State the preparation type.
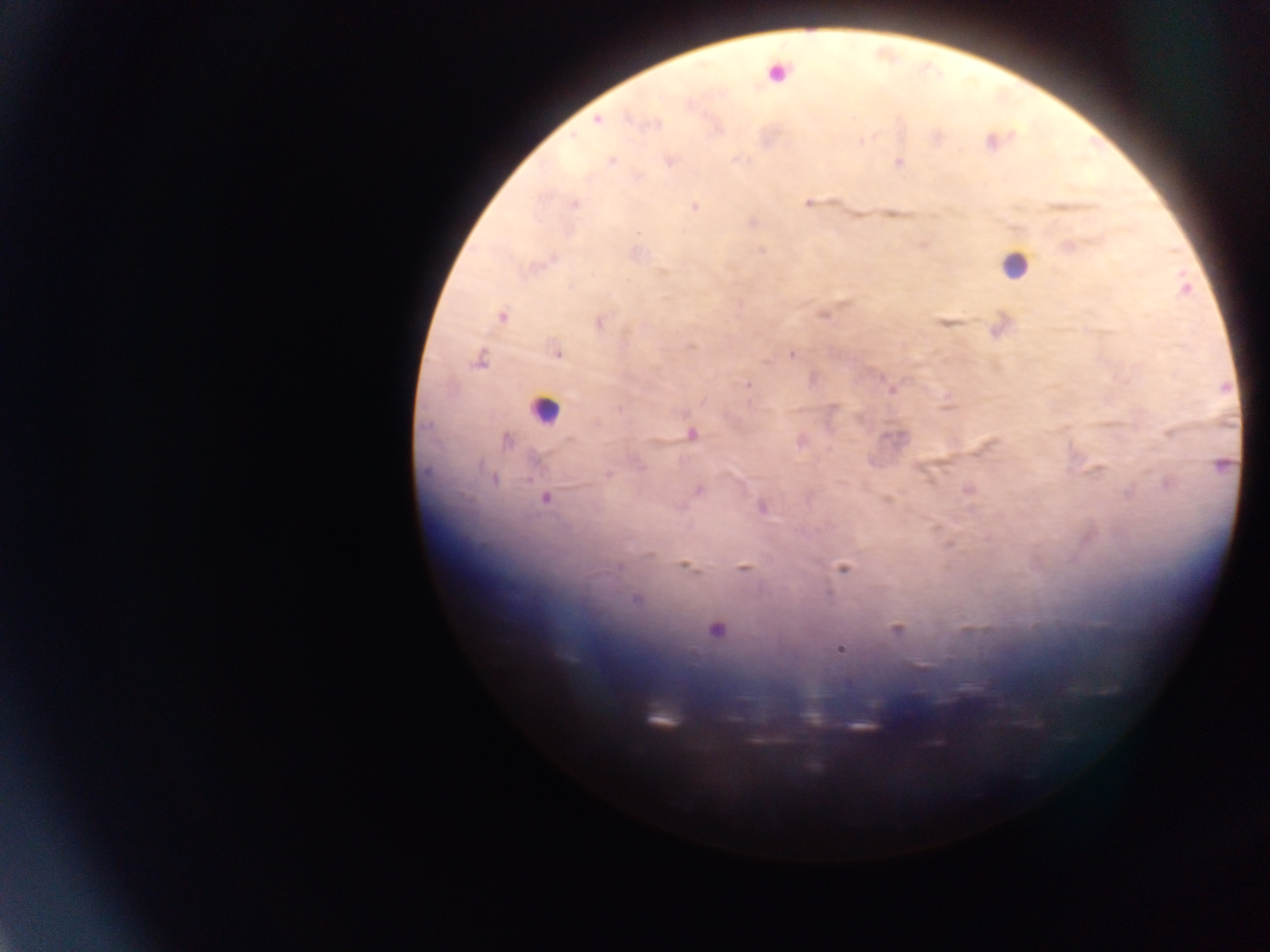

Thick blood film.

Approximate centers as (x, y) in pixels.
Summary:
  - Leukocyte locations: (779, 72), (1015, 264), (544, 409)
  - Malaria parasite locations: (597, 119), (652, 124), (935, 136), (863, 139), (992, 142), (669, 160), (611, 161), (899, 162), (638, 177), (806, 202), (573, 203), (695, 207), (751, 223), (638, 233), (922, 244), (1068, 246), (761, 249), (634, 255), (1184, 288), (822, 312), (501, 317), (599, 322), (946, 323), (999, 325), (555, 350), (791, 354), (480, 359), (813, 379), (747, 386), (890, 388), (947, 404), (832, 408), (691, 434), (506, 439), (800, 440), (1221, 466), (606, 474), (1167, 483), (698, 489), (969, 489), (545, 497), (887, 499), (762, 507), (684, 565), (743, 568), (842, 568), (637, 600), (715, 629), (896, 629), (839, 648)
  - Capture: mobile-phone photograph through a microscope
  - Field of view: single
  - Image size: 1270×952 pixels
  - Country: Ghana